Identify the cell.
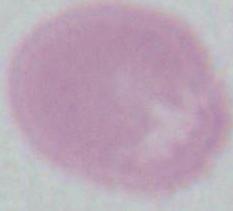
An erythrocyte.

Captured at 1000x magnification. Photomicrograph.